Classify the preparation.
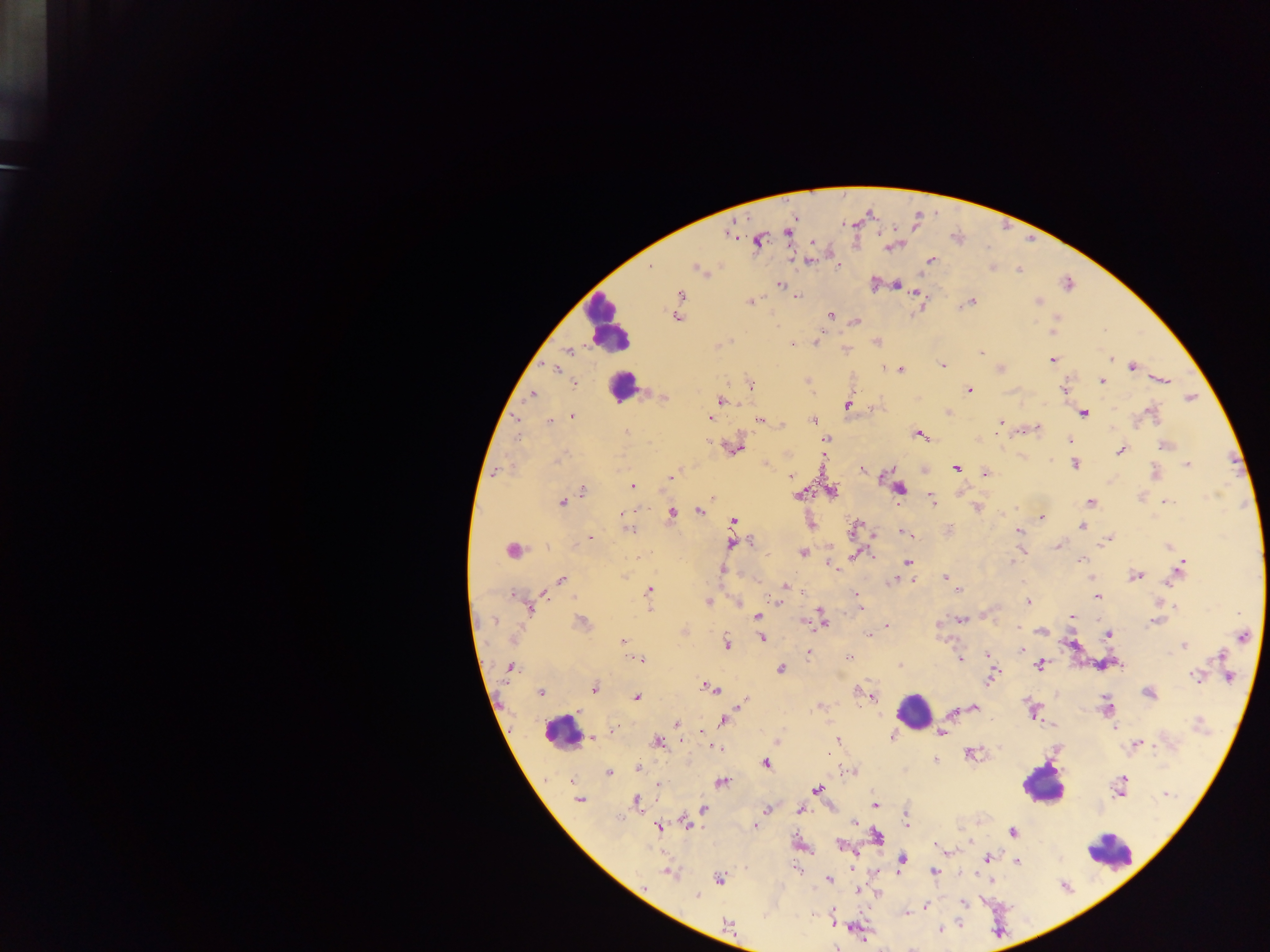
Thick blood film.

Approximate centers as [x, y] in pixels. Plasmodium parasite locations: [787, 233], [758, 242], [889, 247], [809, 261], [930, 261], [838, 266], [696, 269], [1019, 270], [896, 284], [1068, 284], [779, 285], [915, 293], [680, 294], [796, 295], [798, 296], [971, 301], [749, 302], [1037, 302], [678, 310], [831, 316], [677, 317], [1058, 317], [856, 321], [1052, 332], [816, 342], [876, 342], [791, 345], [569, 350], [980, 353], [1111, 358], [1052, 360], [943, 365], [1132, 367], [885, 368], [555, 369], [901, 370], [1164, 380], [1102, 381], [575, 384], [750, 385], [970, 390], [1064, 390], [532, 394], [664, 397], [1190, 398], [721, 401], [848, 405], [948, 412], [1083, 413], [1152, 413], [573, 416], [710, 419], [517, 420], [759, 420], [549, 421], [813, 421], [1001, 422], [1036, 428], [626, 432], [998, 432], [919, 434], [825, 439], [1070, 440], [710, 443], [1165, 445], [735, 449], [1120, 451], [561, 459], [1050, 461], [765, 462], [1075, 464], [1188, 465], [956, 468], [863, 469], [500, 471], [1156, 472], [985, 474], [670, 476], [883, 476], [790, 477], [633, 486], [900, 489], [831, 491], [582, 492], [798, 495], [1142, 497], [931, 500], [1090, 501], [563, 502], [1167, 502], [978, 508], [699, 511], [671, 513], [624, 515], [1042, 518], [733, 521], [1081, 527], [854, 528], [629, 530], [1019, 531], [902, 532], [590, 538], [1107, 541], [732, 542], [750, 542], [1057, 546], [1169, 546], [512, 550], [803, 552], [856, 555], [1080, 560], [1012, 561], [907, 562], [832, 567], [1180, 568], [722, 570], [1136, 575], [945, 577], [1091, 579], [561, 580], [892, 580], [785, 586], [649, 590], [957, 590], [856, 594], [514, 595], [1097, 597], [778, 601], [1028, 601], [708, 602], [737, 603], [860, 607], [1176, 607], [530, 610], [757, 615], [822, 617], [1072, 617], [961, 619], [492, 621], [802, 621], [1155, 621], [582, 623], [887, 625], [1019, 628], [1041, 632], [867, 634], [1109, 634], [1242, 637], [762, 638], [623, 641], [726, 643], [1184, 646], [1021, 650], [808, 653], [988, 654], [850, 656], [1219, 656], [640, 659], [960, 659], [1039, 665], [900, 666], [509, 667], [781, 669], [991, 677], [1196, 677], [1228, 677], [709, 687], [594, 689], [541, 693], [1148, 693], [871, 696], [636, 697], [743, 702], [821, 705], [975, 707], [1107, 707], [954, 712], [724, 720], [676, 724], [1114, 729], [612, 732], [941, 733], [892, 737], [593, 738], [838, 740], [657, 741], [777, 743], [1137, 744], [717, 747], [972, 754], [935, 759], [766, 763], [637, 769], [608, 772], [850, 772], [1122, 781], [723, 782], [658, 784], [818, 789], [1166, 794], [578, 799], [637, 802], [875, 805], [703, 809], [767, 809], [800, 810], [619, 818], [854, 823], [687, 824], [906, 824], [659, 826], [755, 826], [1012, 832], [878, 836], [841, 845], [938, 846], [989, 857], [902, 860], [1018, 862], [853, 868], [934, 871], [669, 873], [720, 878], [829, 879], [697, 895], [964, 903], [925, 906], [906, 914], [958, 922], [727, 923], [939, 930], [836, 947]. Leukocyte locations: [607, 324], [622, 387], [914, 711], [560, 732], [1043, 786], [1111, 852]. One field of view. Mobile-phone photograph taken through the microscope. Image is 1270×952 pixels. Collected in Ghana.